Identify the parasite.
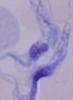

This is a trypanosome.

Micrograph. 1000x magnification.